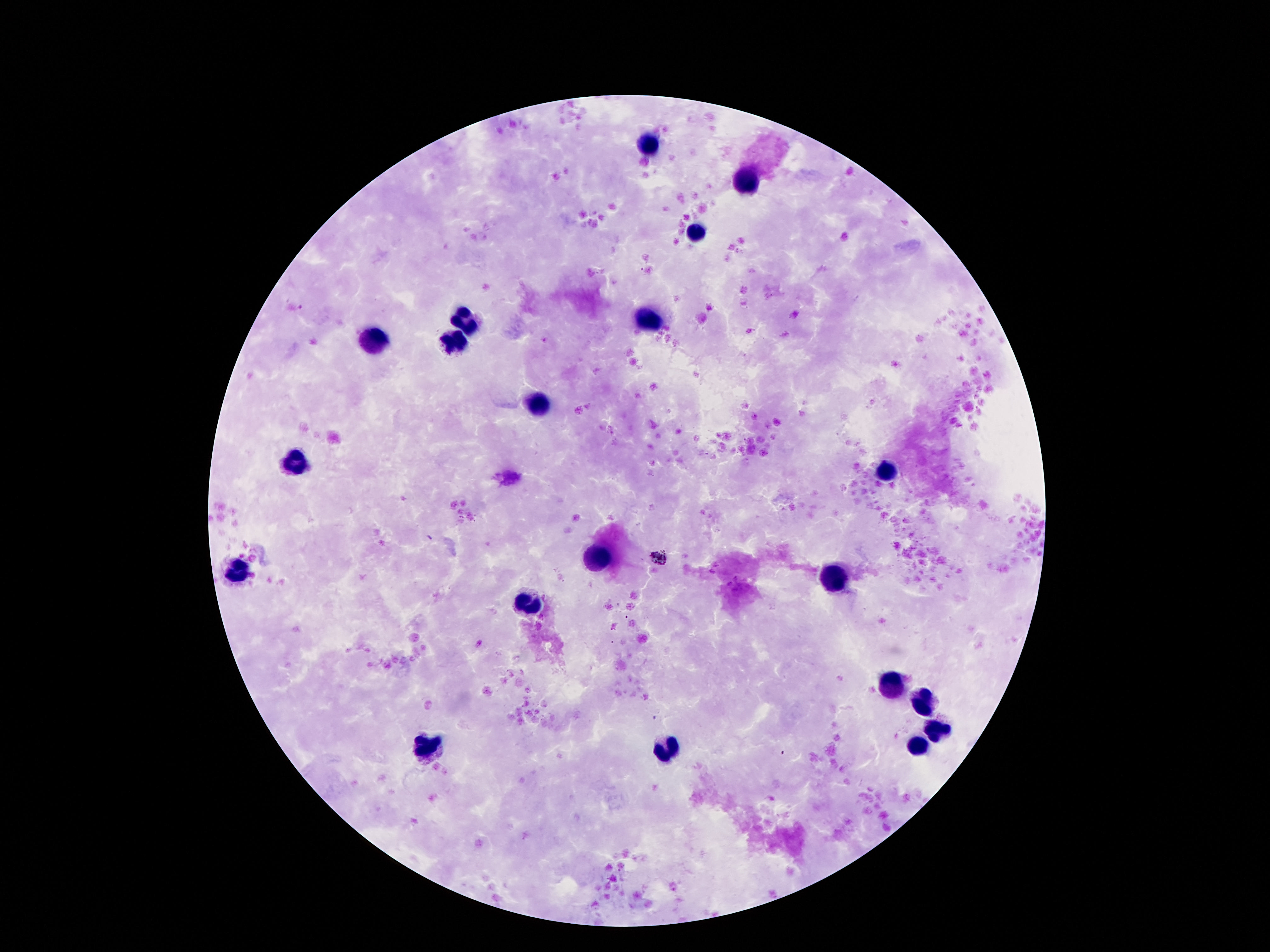 Approximate centers as {x, y} in pixels. Leukocyte locations: {644, 144}, {744, 179}, {697, 232}, {458, 319}, {650, 321}, {374, 340}, {450, 344}, {537, 405}, {295, 465}, {886, 471}, {597, 557}, {237, 570}, {831, 581}, {529, 605}, {889, 683}, {923, 701}, {939, 730}, {671, 745}, {424, 746}, {920, 746}. Image is 1270×952 pixels. 100x magnification. One field from this slide. Giemsa stain. Thick blood film. Photographed through the microscope eyepiece with a smartphone camera. Patient malaria status: not infected.